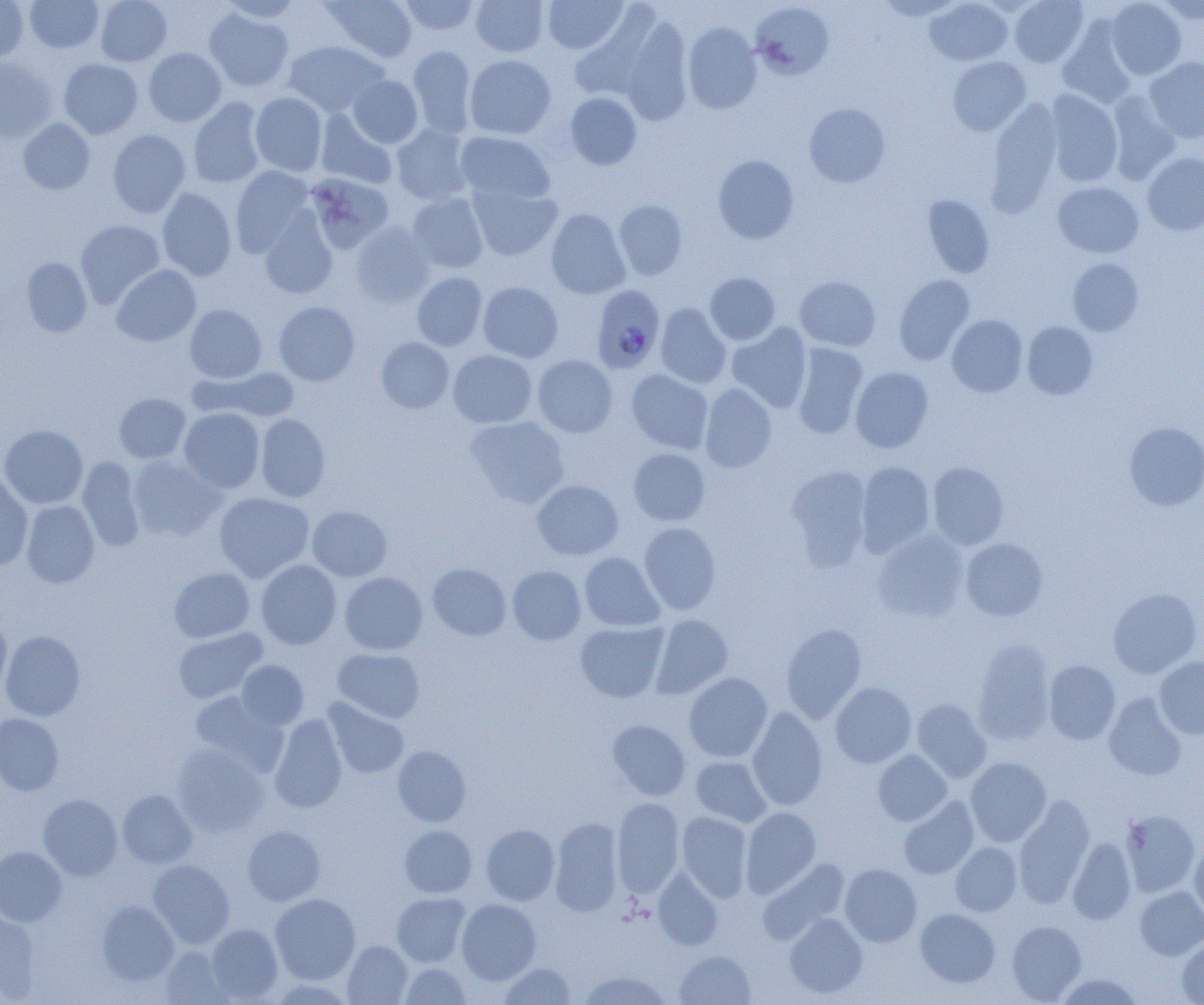

Approximate bounding boxes as (x1,y1)-(x2,y2) corner pairs in pixels. Plasmodium falciparum-infected red blood cell locations: (591,285)-(665,373). Uninfected red blood cell locations: (0,0)-(28,62), (25,0)-(103,53), (95,0)-(172,66), (218,0)-(304,23), (323,0)-(418,63), (400,0)-(480,36), (470,0)-(549,57), (542,0)-(628,54), (875,0)-(964,20), (925,0)-(1012,66), (1009,0)-(1088,67), (1106,0)-(1186,79), (1156,0)-(1204,23), (751,2)-(833,79), (204,8)-(294,92), (620,19)-(693,125), (1058,21)-(1137,108), (682,22)-(762,113), (282,40)-(388,116), (407,45)-(477,136), (144,48)-(226,126), (464,54)-(555,139), (0,56)-(57,144), (948,56)-(1031,135), (1145,57)-(1204,143), (58,58)-(143,139), (347,75)-(423,148), (1043,90)-(1123,187), (565,92)-(642,170), (1107,92)-(1181,185), (250,93)-(328,176), (188,97)-(265,188), (986,100)-(1062,218), (804,103)-(890,187), (316,109)-(398,189), (18,118)-(94,194), (391,124)-(474,205), (107,129)-(191,218), (455,130)-(555,205), (1142,152)-(1204,235), (713,154)-(799,243), (230,166)-(314,257), (305,173)-(394,253), (1053,182)-(1144,258), (468,183)-(563,261), (157,188)-(237,281), (407,192)-(489,273), (922,194)-(995,278), (614,199)-(688,280), (545,208)-(630,299), (259,210)-(338,299), (75,220)-(165,308), (350,221)-(434,308), (22,257)-(92,337), (1067,258)-(1144,336), (111,265)-(201,347), (411,272)-(487,351), (705,273)-(781,345), (894,274)-(975,365), (794,275)-(881,351), (477,281)-(563,363), (274,302)-(360,386), (655,303)-(731,388), (185,304)-(266,383), (947,314)-(1028,397), (1022,321)-(1098,400), (726,322)-(812,412), (376,337)-(454,413), (791,343)-(868,439), (448,350)-(537,428), (532,355)-(617,437), (194,367)-(300,423), (850,367)-(933,453), (627,369)-(713,454), (699,383)-(777,473), (114,393)-(191,463), (179,407)-(265,493), (255,413)-(330,502), (465,416)-(569,508), (1124,421)-(1204,511), (0,424)-(88,509), (628,448)-(710,525), (127,455)-(225,542), (77,456)-(145,552), (856,461)-(935,556), (927,462)-(1009,549), (786,465)-(873,570), (0,471)-(33,570), (531,480)-(623,560), (214,492)-(314,582), (21,500)-(100,588), (307,505)-(392,581), (639,522)-(721,615), (872,530)-(969,622), (960,537)-(1048,621), (579,552)-(664,632), (256,559)-(341,649), (427,563)-(511,641), (507,566)-(586,644), (169,567)-(254,642), (339,571)-(427,655), (1107,587)-(1202,677), (650,614)-(733,699), (0,618)-(12,698), (575,621)-(669,702), (780,623)-(867,722), (173,628)-(267,704), (1,631)-(85,721), (972,638)-(1056,745), (333,648)-(425,722), (1154,657)-(1204,739), (236,660)-(308,729), (1043,660)-(1121,745), (683,672)-(772,763), (830,681)-(916,768), (188,691)-(285,773), (1103,692)-(1187,780), (322,697)-(409,778), (912,699)-(991,783), (747,706)-(828,810), (0,713)-(63,796), (270,713)-(348,813), (607,720)-(691,800), (392,745)-(471,827), (173,746)-(270,836), (873,750)-(952,825), (690,756)-(772,827), (965,757)-(1051,846), (117,789)-(197,868), (39,794)-(123,880), (898,796)-(979,879), (1014,796)-(1095,907), (612,797)-(684,899), (741,807)-(821,897), (1120,810)-(1200,897), (677,811)-(752,902), (549,817)-(624,916), (481,824)-(560,905), (400,825)-(477,897), (242,826)-(325,905), (1067,838)-(1137,925), (1190,840)-(1204,923), (950,842)-(1022,916), (0,846)-(67,927), (759,859)-(851,944), (148,860)-(234,947), (840,863)-(921,946), (653,869)-(723,950), (1135,887)-(1204,960), (392,892)-(471,967), (269,893)-(360,985), (456,899)-(540,984), (97,901)-(178,986), (915,908)-(1000,987), (0,912)-(40,1001), (784,913)-(868,999), (1007,920)-(1087,1003), (205,924)-(283,1003), (1177,936)-(1204,1004), (343,940)-(412,1004), (160,945)-(234,1005), (674,950)-(756,1005), (498,961)-(576,1004), (400,962)-(472,1004), (578,969)-(672,1005), (1055,973)-(1144,1005). Slide-level diagnosis: Plasmodium falciparum. Light microscopy. Captured at 1000x magnification. Image is 1204×1005 pixels. Thin blood smear. Single field of view.